Classify this cell by malaria status.
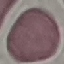
It is uninfected.

preparation = thin blood smear
image type = cell patch, automatically extracted from a larger field of view and resized to 64 × 64 pixels
stain = Giemsa
capture = smartphone through the microscope eyepiece